Locate every malaria parasite.
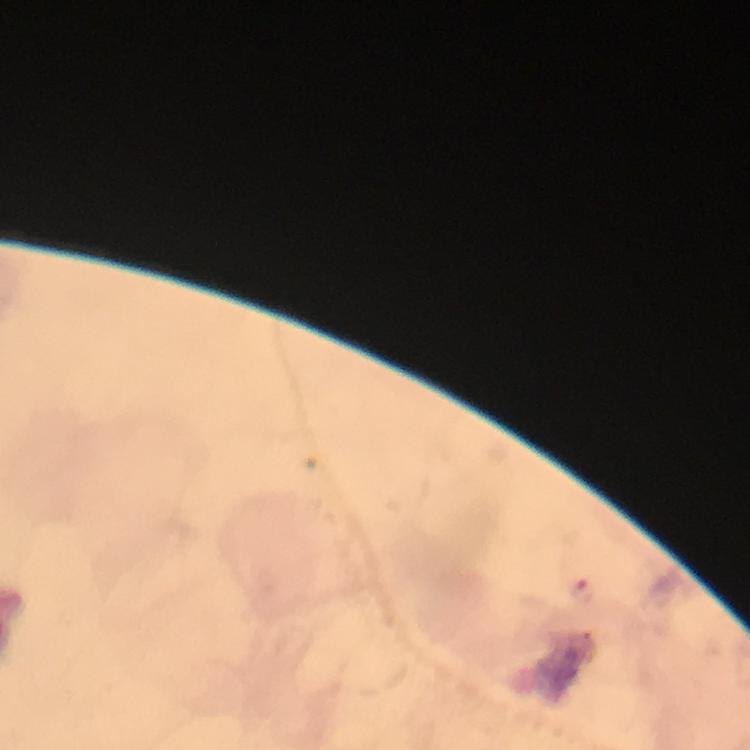
Approximate centers as [x, y] in pixels.
Malaria parasites: [584, 588].

{
  "preparation": "thick smear",
  "stain": "Giemsa",
  "cropped_from": "one field of view",
  "magnification": "100x",
  "image_size": "750×750 pixels",
  "capture": "smartphone photograph through a microscope",
  "immersion_oil": "used",
  "context": "from a diagnostic examination for malaria"
}